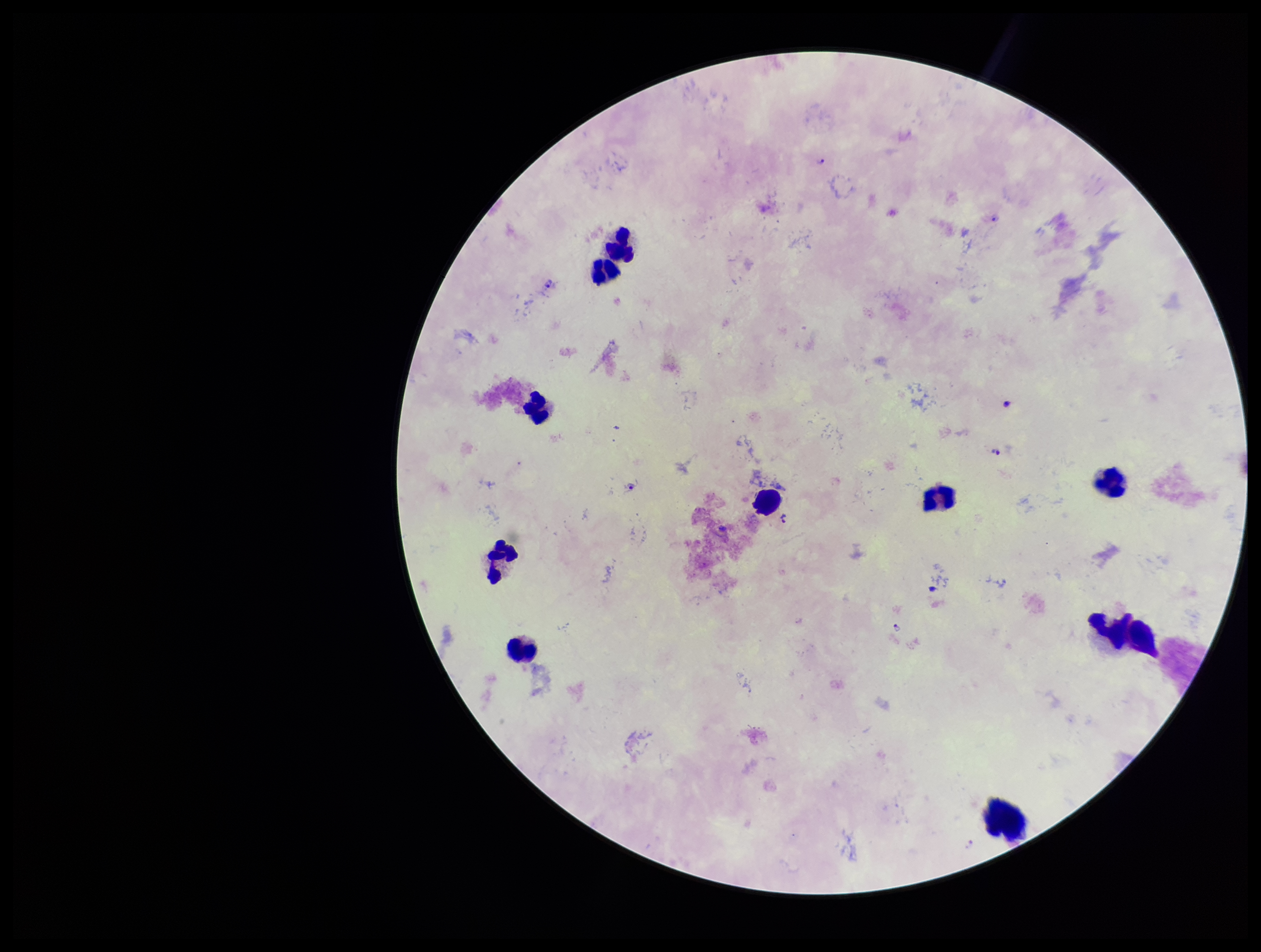

patient_malaria_status: infected
stain: Giemsa
image_size: 1261×952 pixels
plasmodium_parasites: seen
capture: smartphone photograph through the microscope eyepiece
species_reported_for_this_patient: Plasmodium falciparum
preparation: thick smear
leukocyte_count: 10
parasite_count: 7
field_of_view: one from this slide